Report the malaria status of this cell.
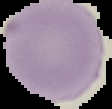

Uninfected.

Summary:
  - Image type: segmented cell region with the area outside set to black
  - Image size: 112×109 pixels
  - Preparation: thin blood smear